Report the malaria status of this cell.
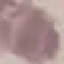

It is uninfected.

Acquired by smartphone through the microscope eyepiece. Giemsa-stained preparation. Thin smear of blood. Cell patch, automatically extracted from a larger field of view and resized to 64 × 64 pixels.